Assess the morphology of the erythrocytes.
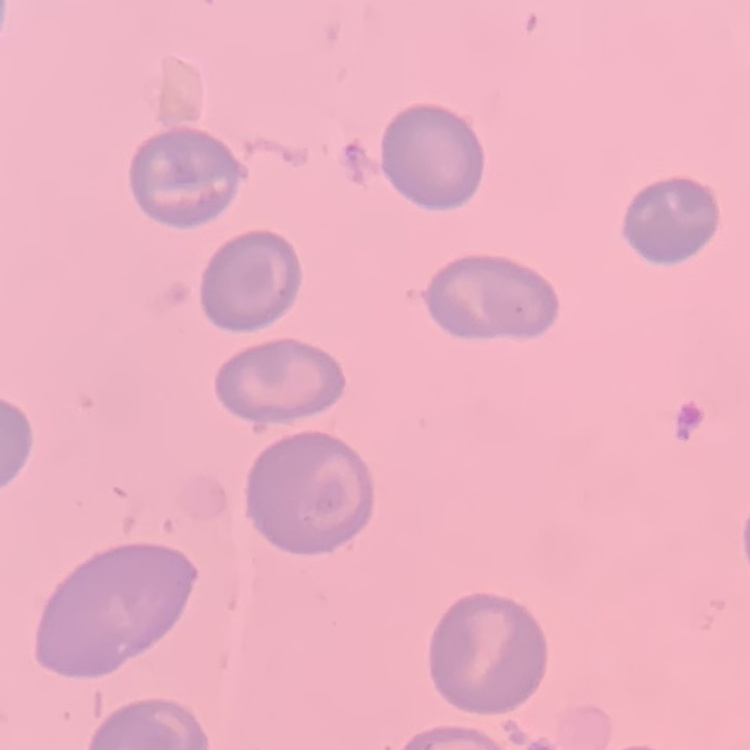
No rouleaux formation.

Stained with either Field's or Giemsa. Thin peripheral smear. One tile cut from a larger photomicrograph.